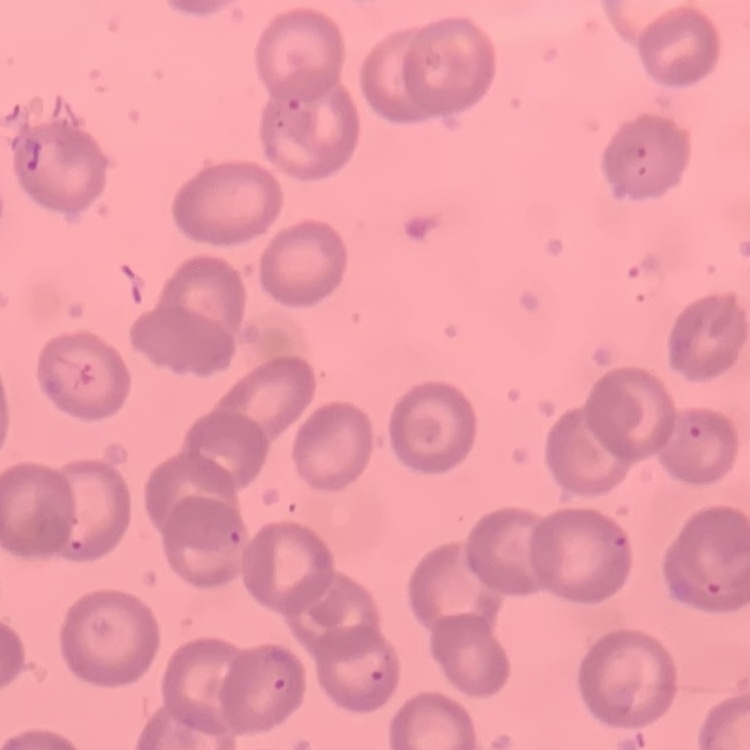

erythrocyte morphology = no rouleaux formation
preparation = thin blood smear
stain = Field's or Giemsa
image type = square crop of a larger photomicrograph